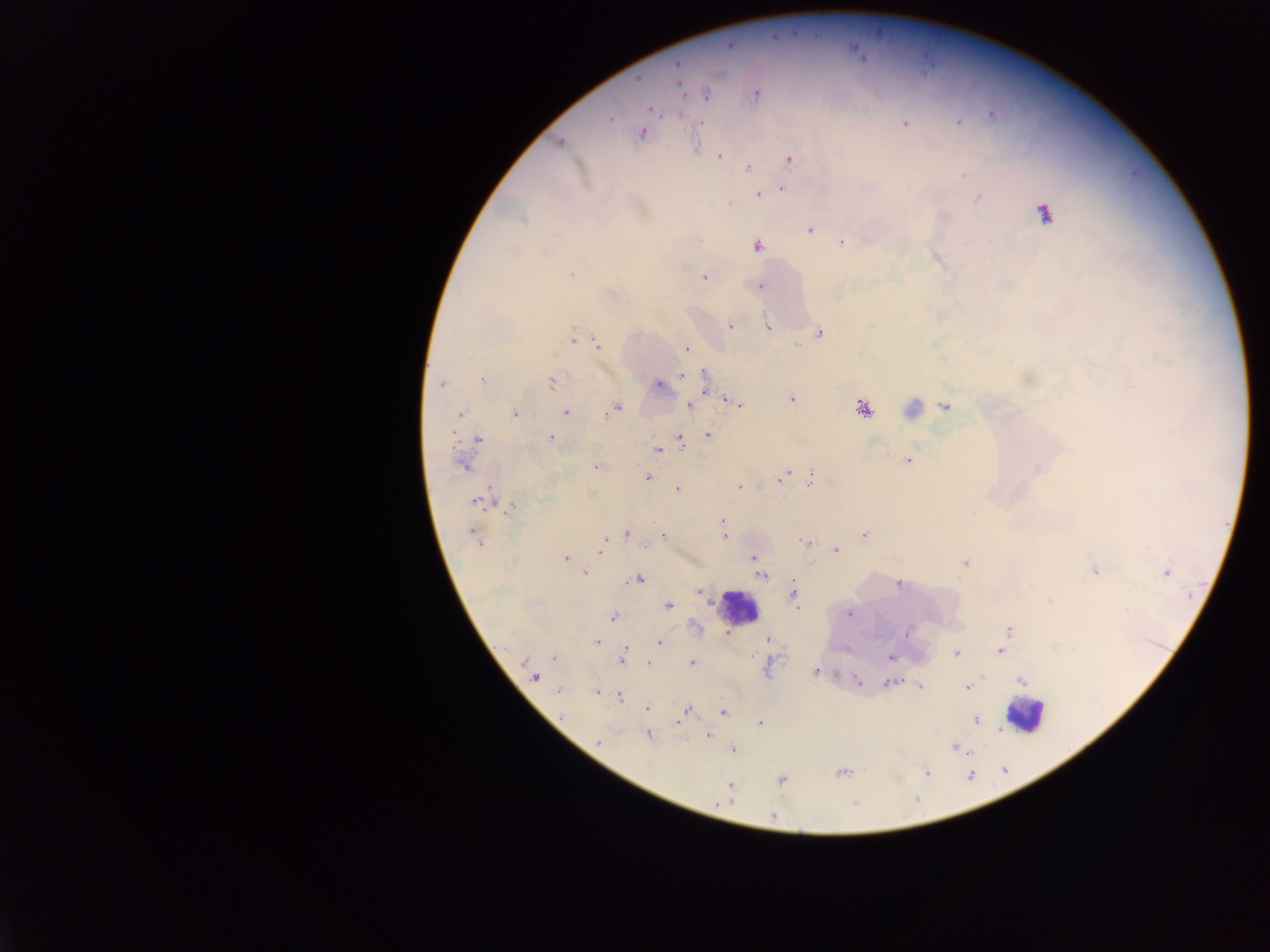
Approximate centers as {x, y} in pixels. Leukocyte locations: {738, 608}, {1024, 714}. Plasmodium parasite locations: {730, 45}, {857, 53}, {678, 65}, {679, 84}, {755, 93}, {705, 94}, {650, 108}, {680, 114}, {610, 118}, {958, 121}, {700, 122}, {904, 122}, {641, 131}, {559, 142}, {697, 146}, {718, 155}, {789, 159}, {747, 168}, {781, 187}, {757, 194}, {979, 197}, {1043, 213}, {809, 229}, {842, 242}, {756, 245}, {571, 273}, {703, 276}, {759, 286}, {730, 325}, {767, 326}, {819, 332}, {573, 339}, {597, 345}, {686, 348}, {682, 375}, {705, 375}, {482, 379}, {551, 382}, {440, 383}, {658, 384}, {704, 386}, {791, 399}, {729, 400}, {740, 404}, {689, 406}, {945, 406}, {863, 407}, {614, 408}, {913, 408}, {565, 412}, {515, 413}, {460, 414}, {708, 435}, {549, 438}, {477, 439}, {680, 439}, {658, 449}, {908, 460}, {463, 465}, {596, 465}, {1038, 468}, {784, 476}, {647, 477}, {811, 478}, {739, 486}, {677, 488}, {483, 500}, {511, 507}, {722, 522}, {625, 533}, {864, 534}, {474, 536}, {662, 536}, {723, 536}, {805, 542}, {601, 547}, {835, 550}, {753, 557}, {565, 558}, {964, 562}, {756, 565}, {1096, 571}, {1166, 572}, {585, 573}, {761, 574}, {638, 578}, {899, 583}, {701, 591}, {793, 594}, {669, 605}, {849, 613}, {612, 617}, {1009, 630}, {726, 631}, {906, 634}, {1005, 638}, {766, 639}, {596, 641}, {659, 642}, {1000, 651}, {956, 653}, {554, 657}, {622, 657}, {890, 657}, {691, 662}, {530, 666}, {815, 671}, {534, 676}, {1021, 679}, {891, 681}, {858, 683}, {919, 686}, {967, 687}, {558, 690}, {596, 692}, {619, 696}, {647, 708}, {686, 710}, {722, 713}, {976, 719}, {678, 722}, {758, 723}, {647, 734}, {709, 735}, {598, 742}, {955, 747}, {732, 749}, {841, 772}, {925, 772}, {781, 780}, {731, 786}, {730, 797}, {772, 815}. One field of view. Collected in Ghana. Image is 1270×952 pixels. Thick blood film. Photographed through a microscope with a mobile-phone camera.